Classify this cell by malaria status.
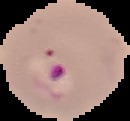
It is parasitized.

Image is 130×121 pixels. Segmented cell region on a black background. From a thin blood film.